Assess this cell for malaria.
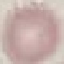
It is uninfected.

Giemsa-stained preparation. Acquired by smartphone through the microscope eyepiece. Thin smear of blood. Cell patch, automatically extracted from a larger field of view and resized to 64 × 64 pixels.